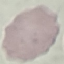
Malaria status: uninfected. Automatically extracted cell patch, resized to 64 × 64 pixels. Acquired by smartphone through the microscope eyepiece. Giemsa stain. Thin smear of blood.